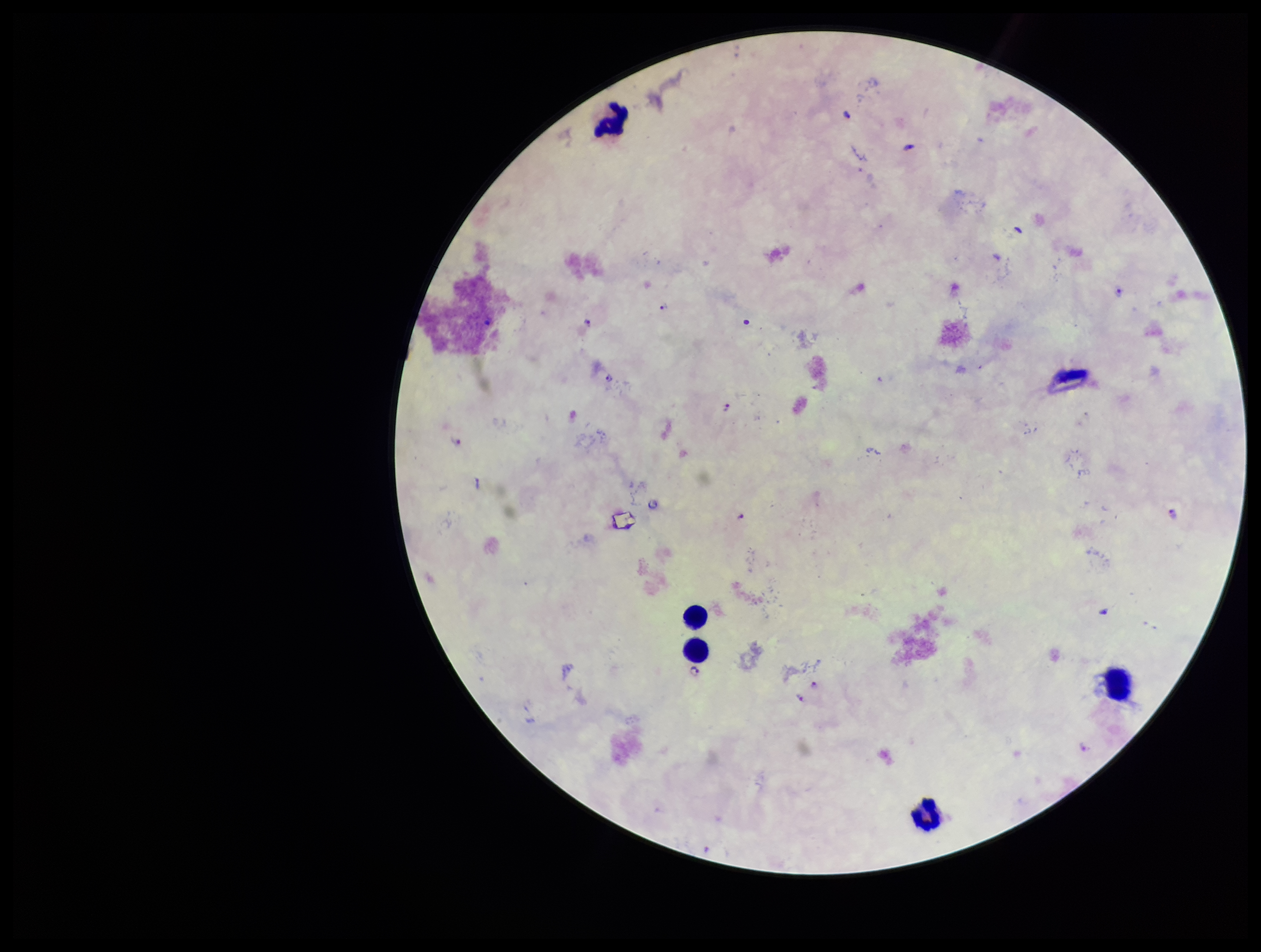
patient malaria status = infected
capture = smartphone photograph through the microscope eyepiece
Plasmodium parasites = detected
leukocyte count = 5
parasite count = 15
species reported for this patient = Plasmodium falciparum
field of view = one from this slide
stain = Giemsa
image size = 1261×952 pixels
preparation = thick smear